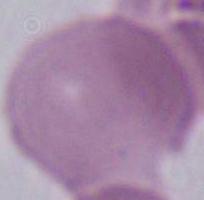

identification = erythrocyte
magnification = 1000x
modality = micrograph